Give the position of every malaria parasite and every leukocyte.
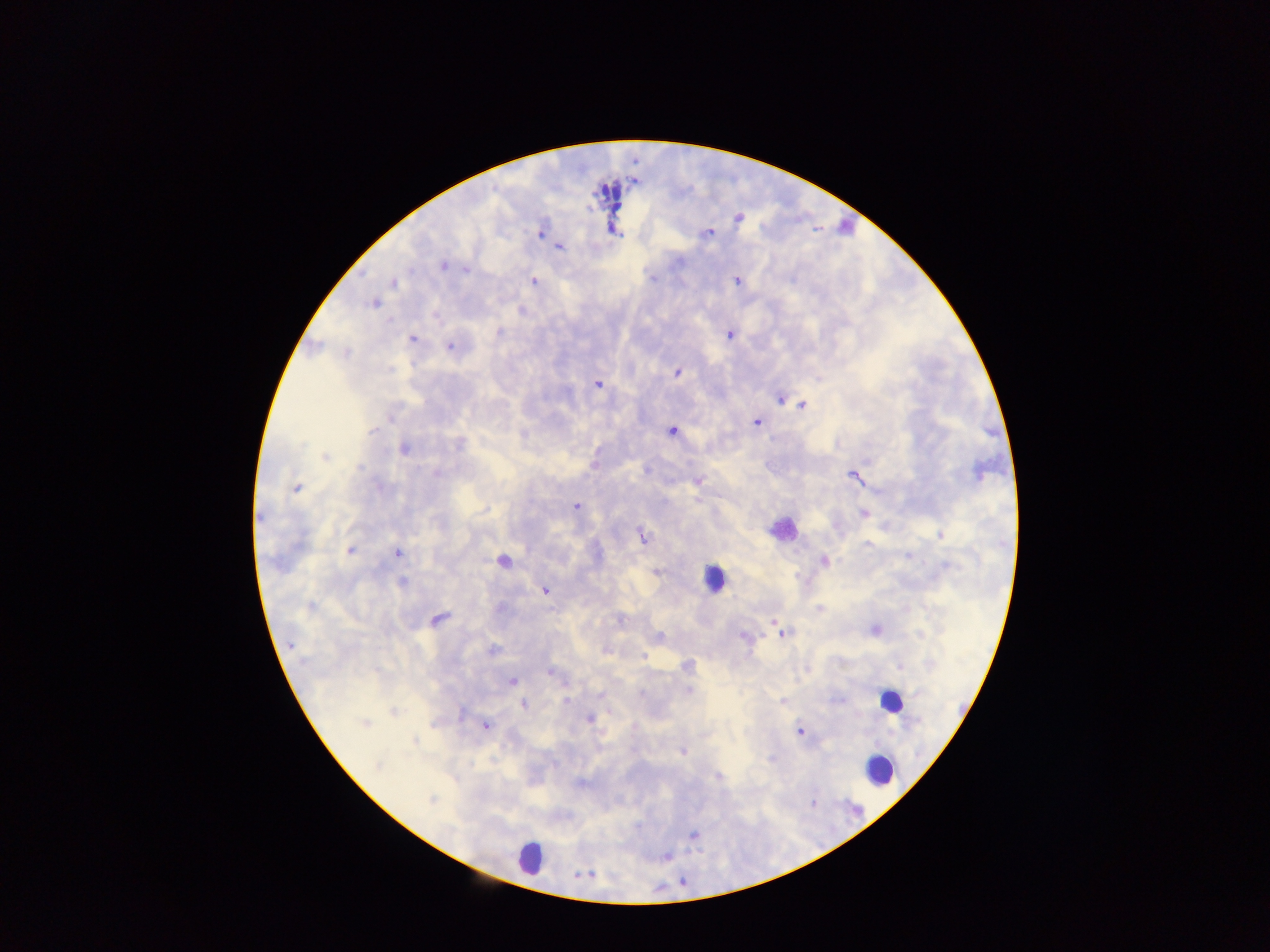
Approximate centers as x y in pixels.
Malaria parasites: 738 218; 707 233; 540 234; 559 246; 679 261; 443 266; 466 270; 652 278; 736 280; 533 281; 392 283; 374 303; 521 311; 499 332; 729 335; 413 339; 449 347; 346 352; 677 373; 598 384; 781 399; 801 405; 394 414; 756 422; 373 430; 671 431; 458 445; 404 449; 326 458; 359 467; 645 471; 977 471; 437 474; 854 476; 697 481; 297 488; 379 488; 576 506; 486 509; 862 513; 260 516; 941 535; 643 537; 868 544; 349 551; 397 554; 908 555; 824 561; 947 566; 655 572; 402 581; 544 590; 311 606; 820 609; 438 619; 619 620; 875 630; 781 632; 919 634; 743 636; 658 637; 291 644; 493 651; 606 652; 687 666; 901 668; 550 672; 512 681; 689 690; 917 693; 600 695; 567 700; 839 700; 783 701; 524 703; 393 713; 461 714; 590 718; 365 723; 486 727; 799 731; 415 741; 683 751; 771 759; 378 766; 718 777; 431 800.
Leukocytes: 847 224; 780 529; 502 564; 713 579; 889 702; 880 772; 527 856.

Image is 1270×952 pixels. Single field of view. Photographed through a microscope with a mobile-phone camera. Sample from Ghana. Thick blood smear.